Classify this cell by malaria status.
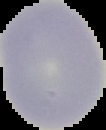

It is uninfected.

Segmented cell region on a black background. Image is 106×130 pixels. From a thin blood film.